Describe the morphology of the red blood cells.
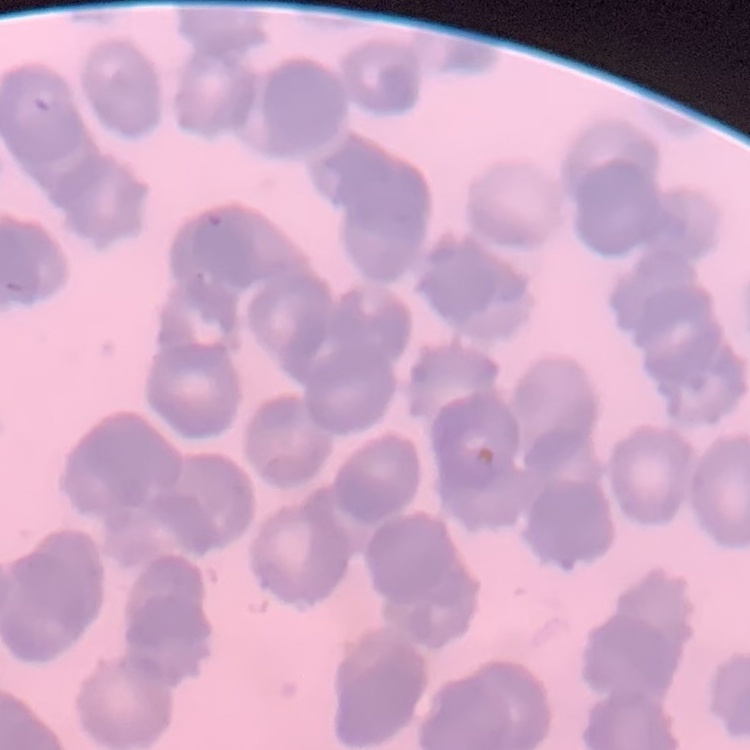

Rouleaux formation.

Summary:
  - Image type: square crop of a larger photomicrograph
  - Preparation: thin peripheral smear
  - Stain: Field's or Giemsa